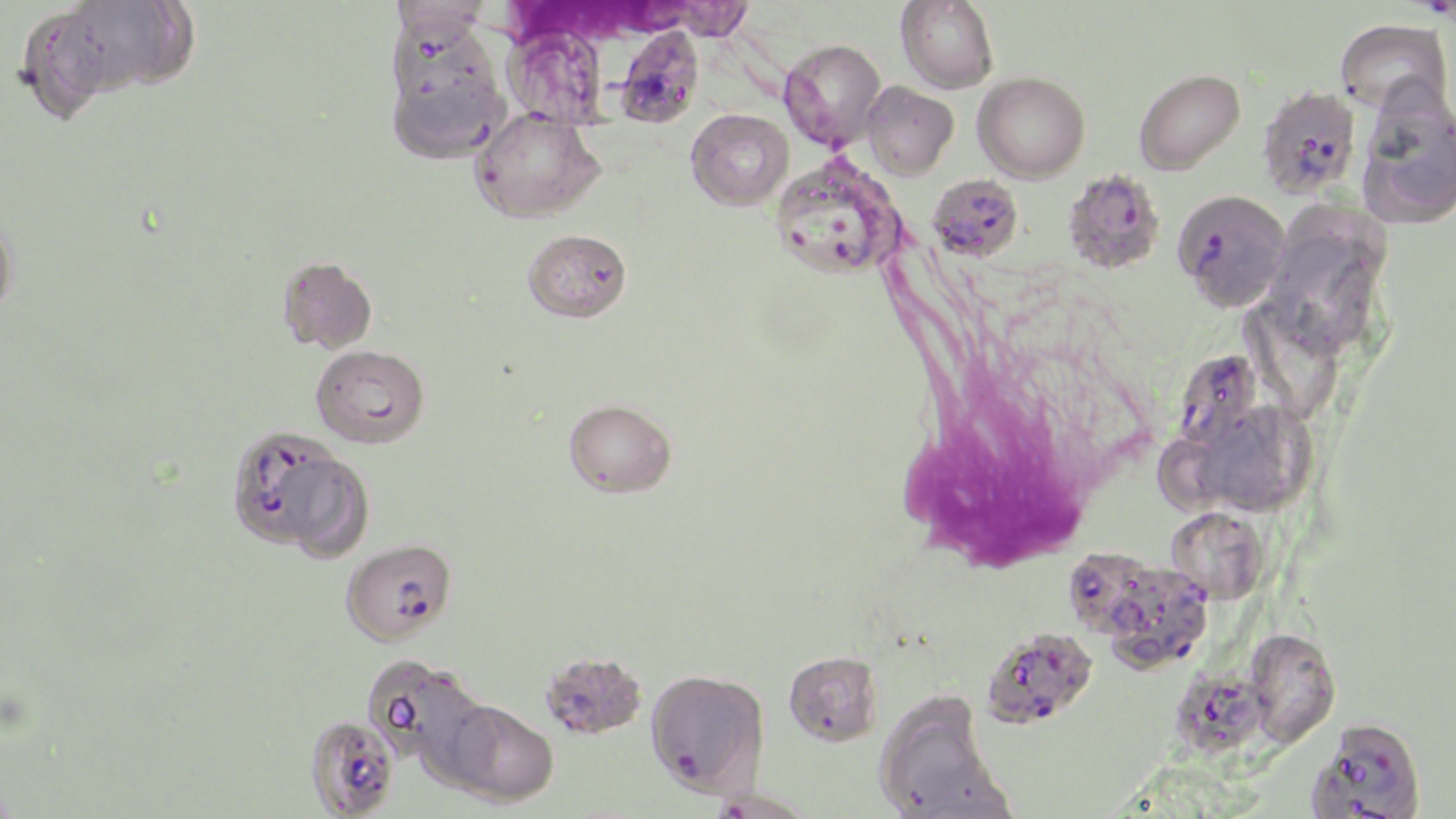
Summary:
  - Coordinate format: approximate bounding boxes as named x1/y1/x2/y2 corners in pixels
  - Uninfected red blood cell locations: (x1=896, y1=0, x2=999, y2=94), (x1=47, y1=1, x2=199, y2=99), (x1=21, y1=15, x2=117, y2=127), (x1=1335, y1=18, x2=1453, y2=117), (x1=382, y1=21, x2=512, y2=165), (x1=502, y1=22, x2=612, y2=129), (x1=779, y1=39, x2=887, y2=152), (x1=1133, y1=68, x2=1245, y2=175), (x1=973, y1=71, x2=1090, y2=182), (x1=862, y1=81, x2=958, y2=180), (x1=1356, y1=92, x2=1456, y2=230), (x1=471, y1=108, x2=605, y2=223), (x1=686, y1=109, x2=793, y2=210), (x1=0, y1=214, x2=18, y2=319), (x1=1264, y1=217, x2=1388, y2=357), (x1=523, y1=229, x2=631, y2=322), (x1=277, y1=256, x2=378, y2=354), (x1=1240, y1=306, x2=1343, y2=425), (x1=564, y1=399, x2=676, y2=497), (x1=1197, y1=403, x2=1314, y2=516), (x1=1153, y1=437, x2=1226, y2=521), (x1=1165, y1=507, x2=1270, y2=606), (x1=1245, y1=631, x2=1340, y2=751), (x1=541, y1=650, x2=646, y2=739), (x1=783, y1=650, x2=883, y2=746), (x1=362, y1=654, x2=486, y2=770), (x1=874, y1=692, x2=1008, y2=818), (x1=435, y1=696, x2=559, y2=807), (x1=705, y1=788, x2=817, y2=818)
  - Plasmodium falciparum-infected red blood cell locations: (x1=617, y1=25, x2=705, y2=127), (x1=1256, y1=84, x2=1362, y2=200), (x1=769, y1=154, x2=905, y2=278), (x1=1062, y1=169, x2=1166, y2=273), (x1=928, y1=173, x2=1023, y2=261), (x1=1174, y1=189, x2=1290, y2=313), (x1=311, y1=344, x2=430, y2=448), (x1=1171, y1=349, x2=1263, y2=455), (x1=224, y1=425, x2=361, y2=554), (x1=340, y1=538, x2=456, y2=646), (x1=1067, y1=548, x2=1165, y2=639), (x1=1111, y1=567, x2=1219, y2=671), (x1=981, y1=627, x2=1098, y2=730), (x1=1163, y1=660, x2=1285, y2=756), (x1=644, y1=668, x2=769, y2=797), (x1=304, y1=714, x2=400, y2=818), (x1=1307, y1=721, x2=1426, y2=818)
  - White blood cell locations: (x1=894, y1=351, x2=1104, y2=579)
  - Slide-level diagnosis: Plasmodium falciparum
  - Preparation: thin blood smear
  - Image size: 1456×819 pixels
  - Modality: optical microscopy
  - Field of view: one of a larger specimen
  - Stain: May-Grünwald-Giemsa
  - Magnification: 1000x